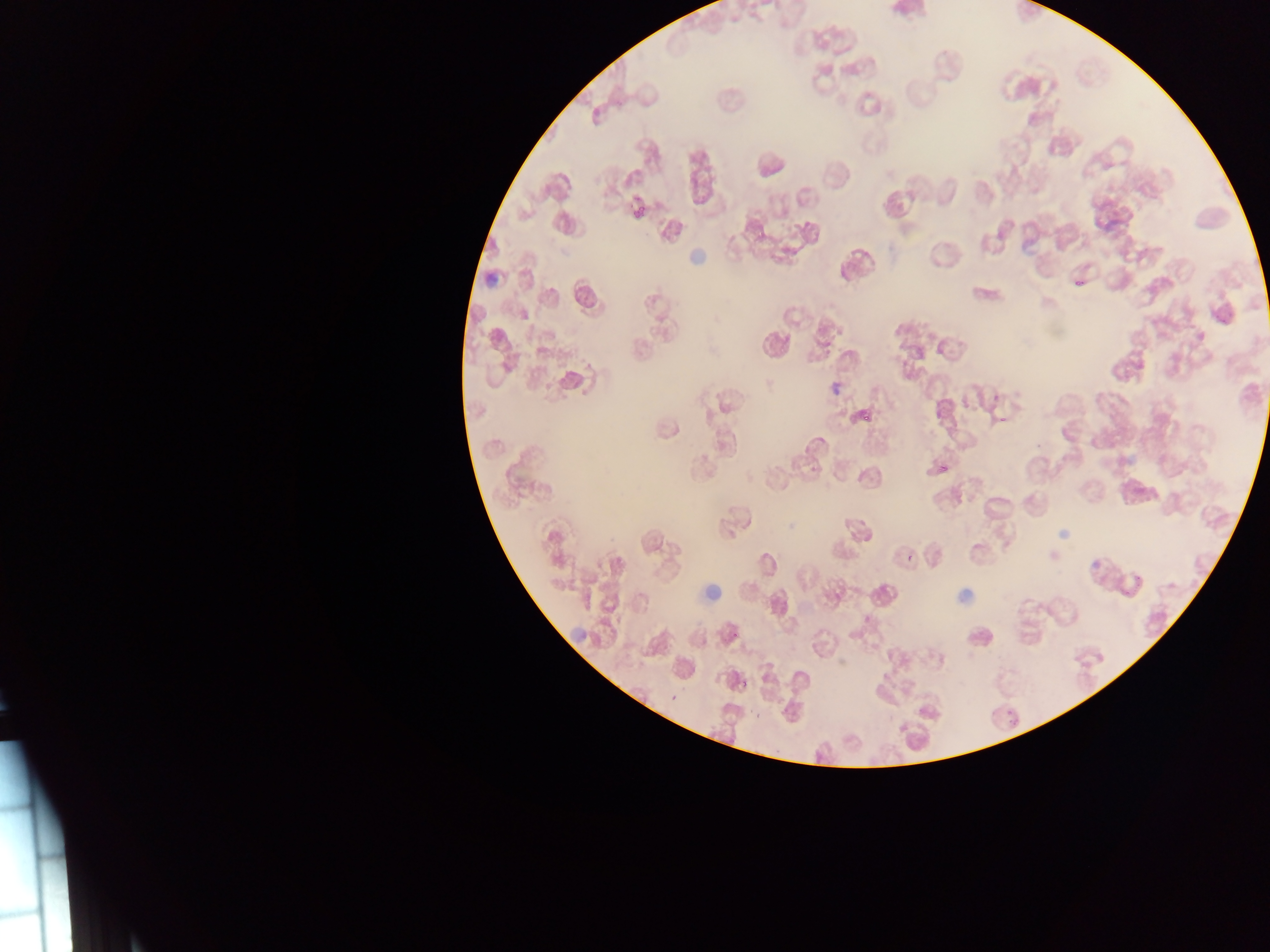

Approximate bounding boxes as {left, top, right, bottom} in pixels. Leukocyte locations: {686, 248, 711, 264}, {697, 585, 723, 602}, {569, 631, 587, 646}. Plasmodium parasite locations: {634, 205, 648, 216}, {1075, 280, 1084, 287}, {865, 412, 874, 422}, {999, 415, 1009, 425}, {1122, 575, 1145, 596}, {732, 631, 740, 640}, {701, 637, 707, 645}, {761, 675, 770, 683}, {740, 679, 749, 689}, {669, 694, 677, 702}, {670, 696, 679, 704}, {753, 711, 762, 720}, {1009, 718, 1016, 727} | approximate {x, y} pixel centers of objects too small to bound: {909, 558}. Sample from Ghana. Single field of view. Image is 1270×952 pixels. Thin blood film. Mobile-phone photograph taken through the microscope.